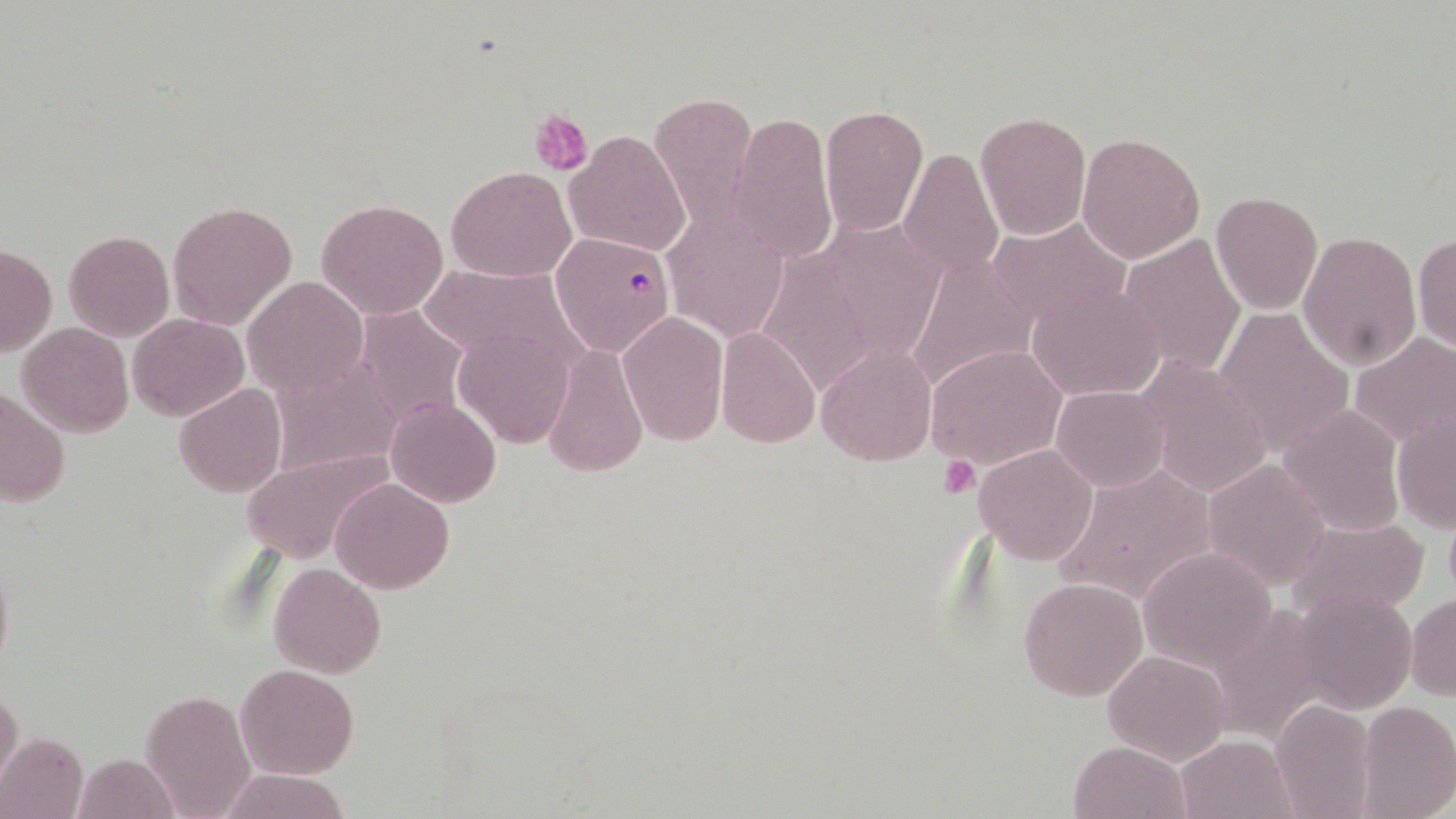
Plasmodium falciparum-infected red blood cell locations = approximate bounding boxes as [x1, y1, x2, y2] in pixels: [550, 231, 675, 358]
slide-level diagnosis = Plasmodium falciparum
preparation = thin blood film
image size = 1456×819 pixels
stain = May-Grünwald-Giemsa
field of view = single
uninfected red blood cell locations = approximate bounding boxes as [x1, y1, x2, y2] in pixels: [649, 90, 758, 231], [819, 103, 929, 236], [728, 109, 836, 263], [974, 111, 1090, 240], [563, 129, 691, 259], [1076, 132, 1205, 264], [900, 145, 1004, 283], [446, 166, 575, 282], [1210, 190, 1323, 314], [316, 198, 448, 320], [166, 200, 297, 329], [662, 211, 789, 342], [985, 216, 1132, 327], [63, 230, 174, 342], [1297, 230, 1421, 372], [1413, 231, 1456, 353], [1118, 233, 1247, 378], [1, 244, 56, 359], [905, 252, 1037, 392], [416, 264, 585, 370], [243, 277, 367, 394], [1028, 283, 1168, 402], [352, 304, 470, 430], [1213, 309, 1354, 454], [617, 311, 728, 447], [127, 314, 247, 419], [18, 322, 133, 437], [714, 326, 820, 447], [452, 329, 575, 447], [1349, 332, 1456, 450], [816, 342, 937, 466], [541, 343, 647, 479], [925, 344, 1065, 468], [1136, 354, 1273, 498], [268, 358, 402, 479], [173, 384, 287, 498], [1052, 385, 1171, 491], [1, 387, 69, 507], [386, 399, 501, 507], [1278, 404, 1406, 537], [1391, 410, 1456, 531], [973, 444, 1097, 565], [239, 451, 389, 564], [1202, 458, 1330, 591], [1054, 464, 1219, 611], [331, 477, 454, 592], [1289, 516, 1425, 620], [1138, 544, 1279, 669], [0, 551, 13, 677], [269, 564, 386, 679], [1018, 576, 1150, 701], [1290, 589, 1416, 712], [1407, 594, 1456, 701], [1102, 648, 1232, 765], [235, 664, 359, 780], [0, 686, 23, 793], [140, 690, 257, 817], [1271, 699, 1377, 819], [1354, 701, 1456, 819], [0, 730, 89, 819], [1174, 733, 1301, 819], [1068, 740, 1191, 819], [71, 752, 182, 819], [216, 767, 352, 819]
magnification = 1000x
platelet locations = approximate bounding boxes as [x1, y1, x2, y2] in pixels: [532, 110, 592, 175], [938, 455, 981, 499]
modality = light microscopy